Locate every blood parasite and identify its species.
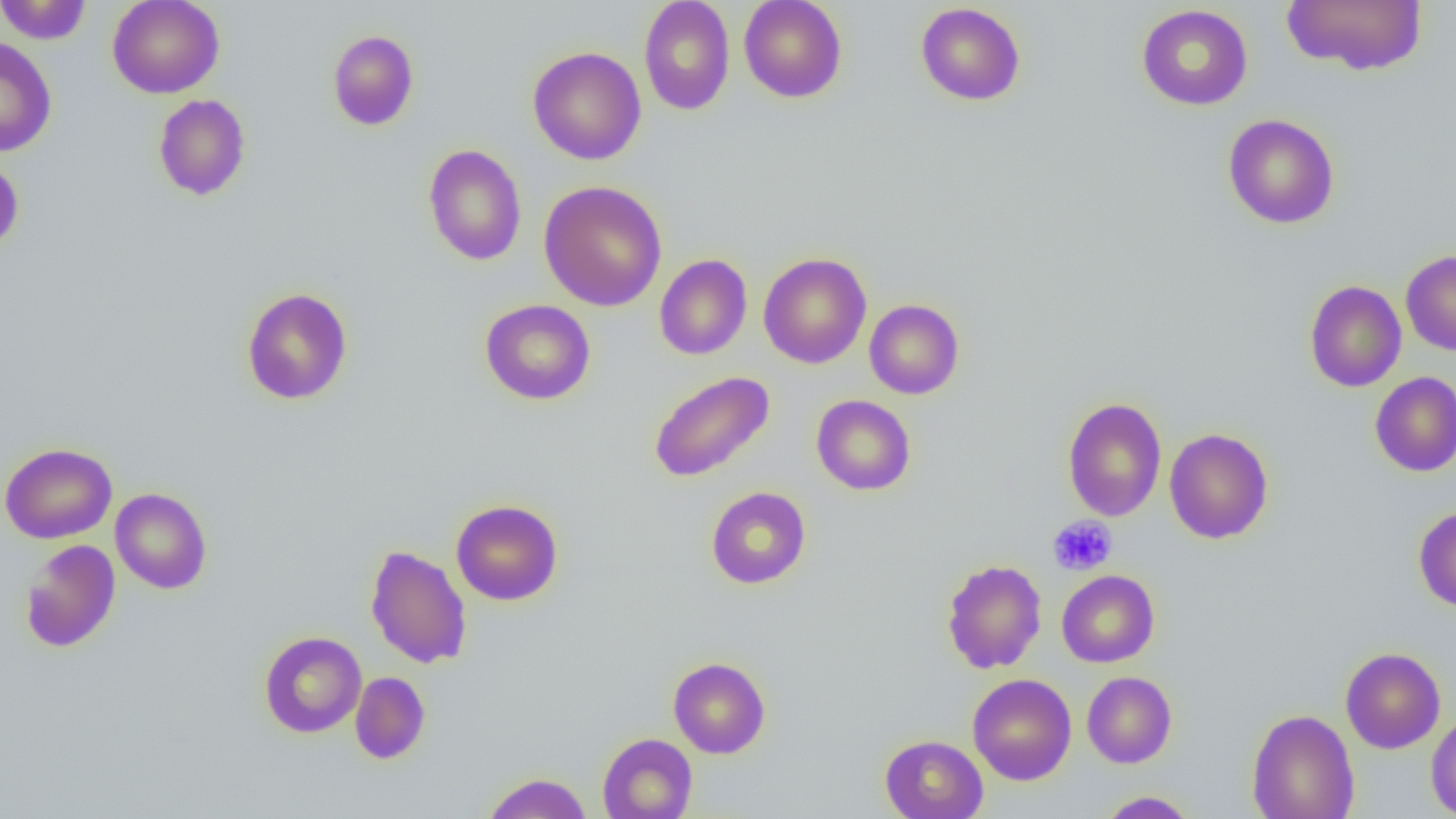
No blood parasites seen.

slide-level diagnosis = no evidence of blood parasites
magnification = 1000x
modality = light microscopy
field of view = one of a larger specimen
uninfected red blood cell locations = approximate bounding boxes as [x1, y1, x2, y2] in pixels: [0, 0, 92, 44], [107, 0, 224, 99], [639, 0, 735, 115], [739, 0, 847, 103], [1281, 0, 1428, 76], [915, 2, 1026, 106], [1136, 4, 1253, 110], [327, 30, 419, 130], [0, 38, 57, 157], [527, 46, 646, 165], [153, 94, 251, 201], [1223, 114, 1340, 229], [423, 144, 527, 265], [0, 156, 24, 255], [538, 180, 667, 311], [1401, 250, 1456, 355], [758, 252, 872, 368], [654, 254, 752, 360], [1304, 280, 1407, 392], [241, 287, 353, 405], [480, 298, 596, 405], [864, 299, 964, 399], [648, 370, 775, 483], [1370, 371, 1456, 476], [811, 395, 916, 495], [1062, 397, 1167, 521], [1163, 427, 1274, 544], [0, 442, 118, 544], [705, 486, 811, 589], [110, 488, 212, 594], [451, 499, 563, 605], [1413, 505, 1456, 612], [19, 539, 120, 653], [365, 544, 472, 669], [941, 559, 1047, 674], [1057, 570, 1159, 667], [259, 630, 366, 738], [1340, 647, 1446, 754], [668, 657, 771, 758], [1081, 671, 1177, 768], [350, 672, 430, 764], [968, 674, 1077, 785], [1246, 708, 1360, 819], [1425, 711, 1456, 818], [597, 733, 697, 818], [880, 734, 988, 819], [482, 772, 592, 818], [1096, 790, 1199, 818]
image size = 1456×819 pixels
platelet locations = approximate bounding boxes as [x1, y1, x2, y2] in pixels: [1047, 515, 1117, 576]
preparation = thin blood smear